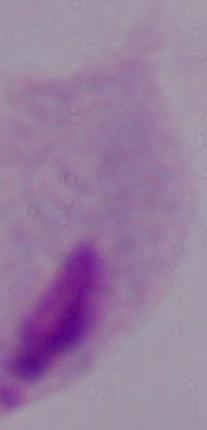
{
  "magnification": "1000x",
  "modality": "photomicrograph",
  "identification": "trichomonad"
}